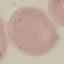

{
  "malaria_status": "uninfected",
  "capture": "smartphone camera at the microscope eyepiece",
  "preparation": "thin blood smear",
  "stain": "Giemsa",
  "image_type": "automatically extracted cell patch, resized to 64 × 64 pixels"
}